Locate every blood parasite and identify its species.
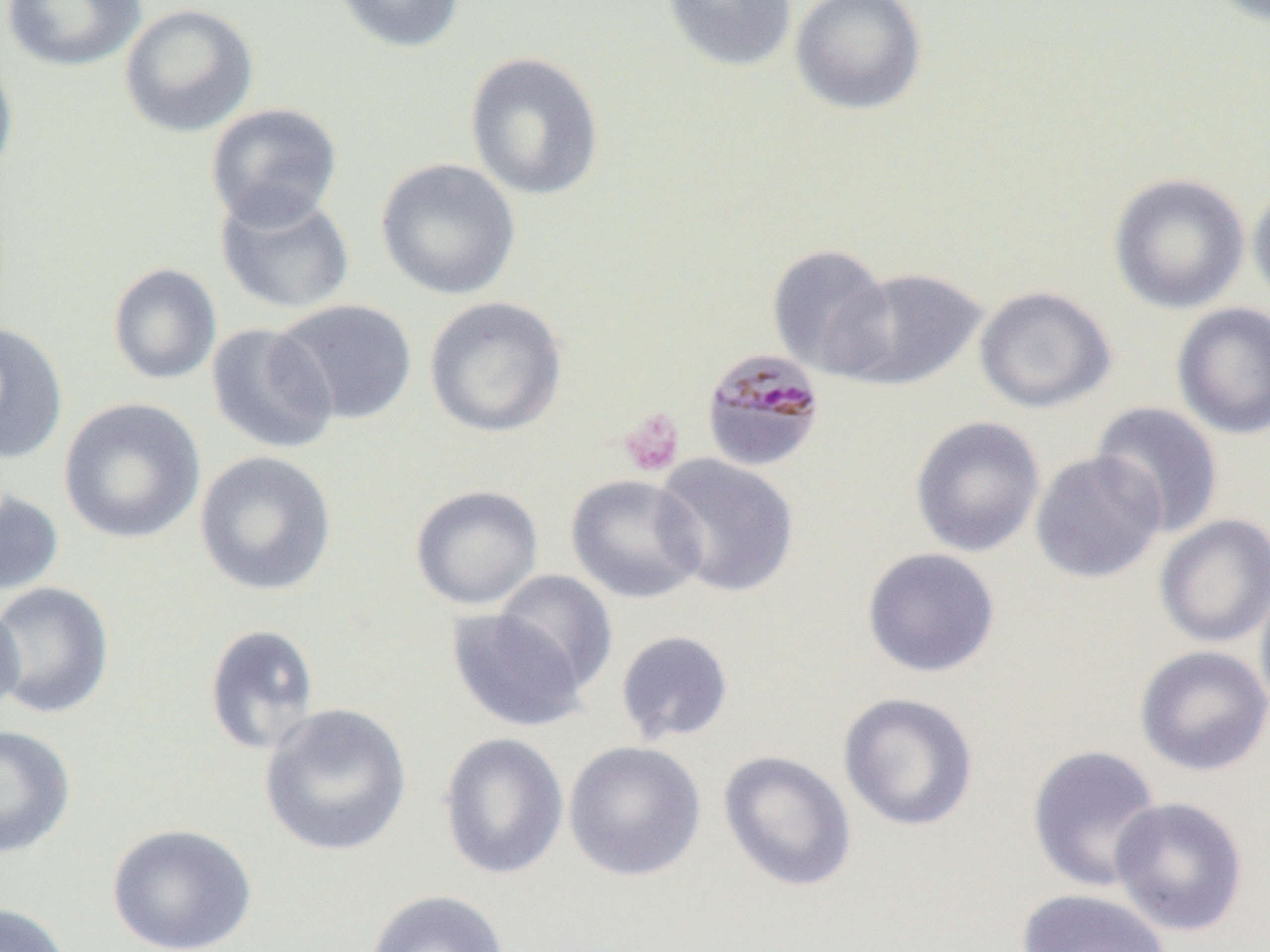

Approximate bounding boxes as named x1/y1/x2/y2 corners in pixels.
Plasmodium malariae-infected red blood cells: (x1=701, y1=347, x2=826, y2=472).
No Plasmodium falciparum, Plasmodium ovale, Plasmodium vivax, Babesia divergens, or Trypanosoma brucei observed.

slide-level diagnosis = Plasmodium malariae
preparation = thin blood smear
field of view = one of a larger specimen
uninfected red blood cell locations = approximate bounding boxes as named x1/y1/x2/y2 corners in pixels: (x1=1, y1=0, x2=147, y2=73), (x1=331, y1=0, x2=466, y2=54), (x1=660, y1=0, x2=798, y2=73), (x1=790, y1=0, x2=928, y2=117), (x1=1204, y1=0, x2=1270, y2=27), (x1=118, y1=3, x2=260, y2=138), (x1=0, y1=48, x2=19, y2=189), (x1=463, y1=51, x2=606, y2=202), (x1=205, y1=102, x2=344, y2=230), (x1=376, y1=157, x2=521, y2=300), (x1=1108, y1=172, x2=1250, y2=314), (x1=1247, y1=180, x2=1270, y2=311), (x1=215, y1=187, x2=355, y2=316), (x1=766, y1=243, x2=898, y2=379), (x1=107, y1=262, x2=222, y2=385), (x1=836, y1=267, x2=988, y2=391), (x1=973, y1=286, x2=1117, y2=413), (x1=423, y1=295, x2=568, y2=439), (x1=273, y1=299, x2=418, y2=426), (x1=1171, y1=301, x2=1270, y2=440), (x1=0, y1=322, x2=69, y2=465), (x1=205, y1=322, x2=338, y2=455), (x1=58, y1=397, x2=206, y2=544), (x1=1090, y1=401, x2=1225, y2=537), (x1=909, y1=415, x2=1046, y2=558), (x1=194, y1=451, x2=338, y2=597), (x1=1029, y1=451, x2=1166, y2=584), (x1=651, y1=453, x2=801, y2=598), (x1=565, y1=473, x2=707, y2=604), (x1=410, y1=485, x2=544, y2=610), (x1=0, y1=489, x2=65, y2=596), (x1=1154, y1=514, x2=1270, y2=648), (x1=861, y1=547, x2=1001, y2=678), (x1=492, y1=570, x2=618, y2=694), (x1=1255, y1=576, x2=1270, y2=722), (x1=0, y1=581, x2=115, y2=719), (x1=0, y1=594, x2=25, y2=724), (x1=445, y1=607, x2=592, y2=732), (x1=203, y1=623, x2=320, y2=757), (x1=615, y1=630, x2=734, y2=745), (x1=1134, y1=645, x2=1270, y2=776), (x1=837, y1=692, x2=979, y2=832), (x1=259, y1=702, x2=413, y2=857), (x1=0, y1=724, x2=76, y2=859), (x1=438, y1=732, x2=570, y2=881), (x1=563, y1=740, x2=706, y2=882), (x1=1027, y1=744, x2=1164, y2=892), (x1=718, y1=750, x2=857, y2=892), (x1=1109, y1=797, x2=1249, y2=937), (x1=106, y1=823, x2=257, y2=952), (x1=1017, y1=888, x2=1172, y2=952), (x1=363, y1=889, x2=511, y2=952), (x1=0, y1=902, x2=73, y2=952)
image size = 1270×952 pixels
platelet locations = approximate bounding boxes as named x1/y1/x2/y2 corners in pixels: (x1=618, y1=408, x2=685, y2=477)
modality = light microscopy
magnification = 1000x